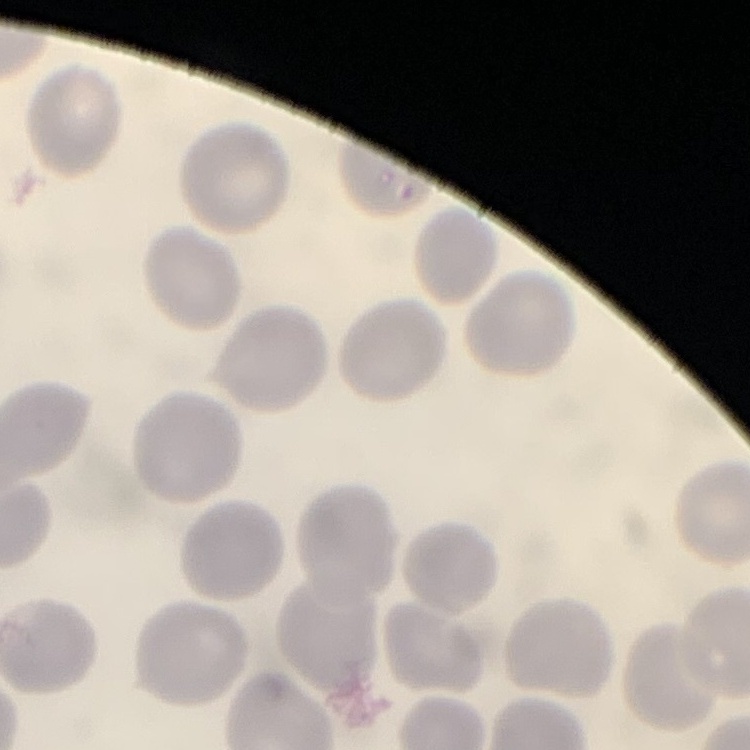

red blood cell morphology = no rouleaux formation
stain = Field's or Giemsa
preparation = thin blood film
image type = one tile cut from a larger photomicrograph